Name the parasite shown.
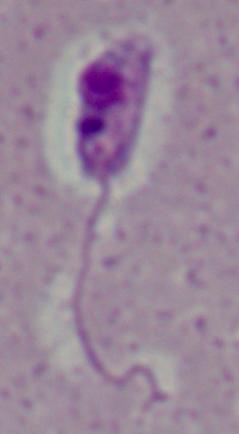
Leishmania.

Photomicrograph. 1000x magnification.